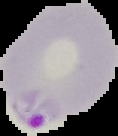

From a thin blood smear. Image is 118×136 pixels. Result: malaria parasites identified. The area outside the segmented cell region is set to black.